Identify the blood parasite species.
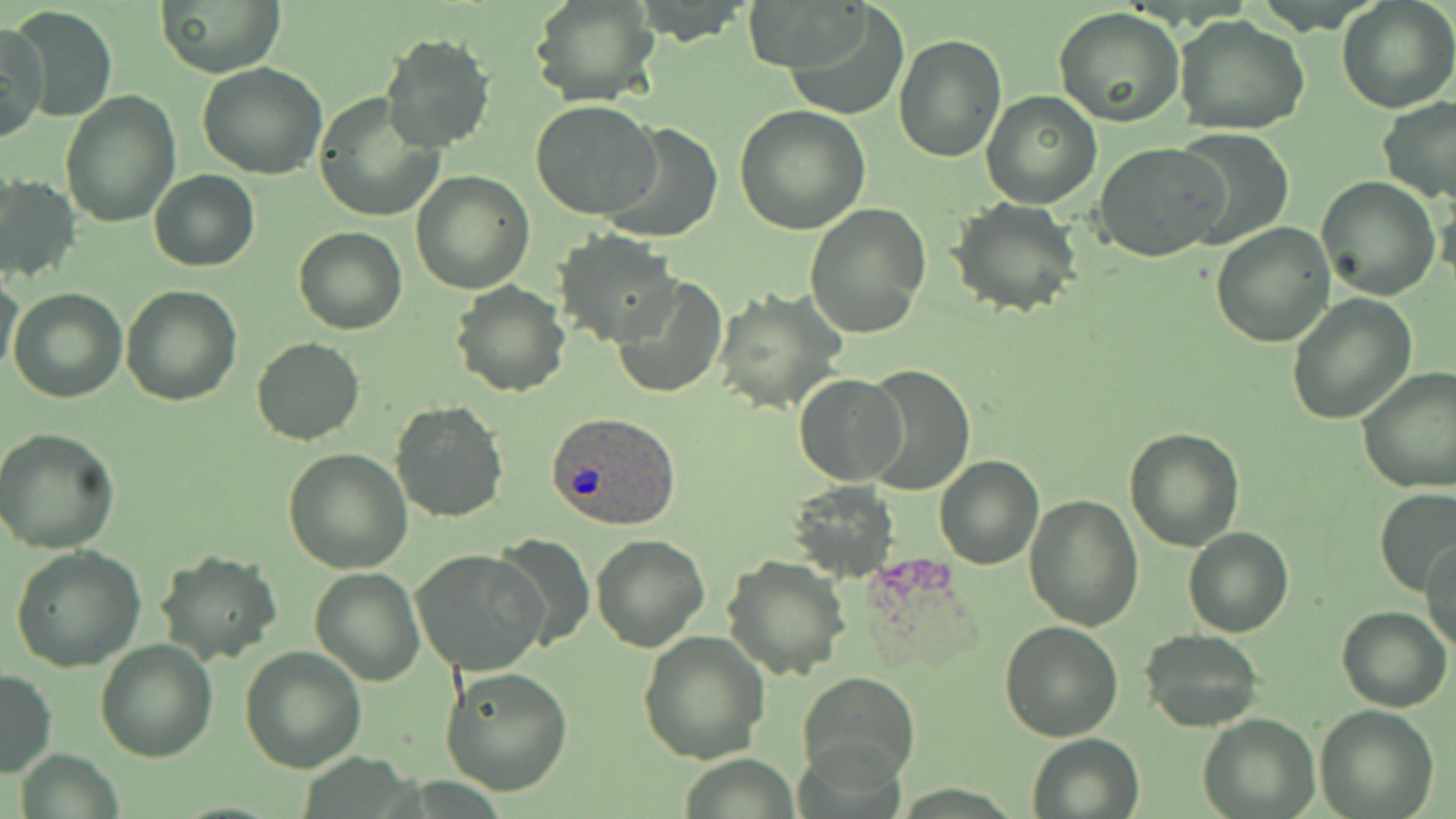

Plasmodium ovale.

{
  "preparation": "thin blood smear",
  "magnification": "1000x",
  "plasmodium_ovale_infected_red_blood_cell_locations": "approximate bounding boxes as named x1/y1/x2/y2 corners in pixels: (x1=547, y1=411, x2=682, y2=533)",
  "uninfected_red_blood_cell_locations": "approximate bounding boxes as named x1/y1/x2/y2 corners in pixels: (x1=745, y1=0, x2=873, y2=74), (x1=1337, y1=0, x2=1455, y2=112), (x1=154, y1=1, x2=287, y2=77), (x1=530, y1=1, x2=659, y2=108), (x1=784, y1=3, x2=911, y2=120), (x1=9, y1=6, x2=116, y2=124), (x1=1053, y1=8, x2=1186, y2=129), (x1=1174, y1=15, x2=1312, y2=136), (x1=1, y1=20, x2=48, y2=143), (x1=379, y1=33, x2=496, y2=153), (x1=892, y1=34, x2=1007, y2=162), (x1=197, y1=63, x2=329, y2=180), (x1=980, y1=89, x2=1104, y2=209), (x1=61, y1=92, x2=181, y2=228), (x1=313, y1=95, x2=444, y2=224), (x1=1377, y1=95, x2=1456, y2=204), (x1=531, y1=100, x2=661, y2=221), (x1=734, y1=104, x2=870, y2=234), (x1=602, y1=122, x2=723, y2=241), (x1=1168, y1=127, x2=1295, y2=250), (x1=1095, y1=142, x2=1226, y2=260), (x1=149, y1=169, x2=260, y2=272), (x1=410, y1=171, x2=534, y2=295), (x1=1, y1=174, x2=81, y2=284), (x1=1315, y1=177, x2=1440, y2=300), (x1=1434, y1=181, x2=1456, y2=285), (x1=948, y1=198, x2=1081, y2=317), (x1=804, y1=203, x2=931, y2=339), (x1=1211, y1=223, x2=1335, y2=348), (x1=293, y1=226, x2=406, y2=335), (x1=554, y1=232, x2=679, y2=346), (x1=0, y1=269, x2=24, y2=378), (x1=611, y1=275, x2=726, y2=399), (x1=450, y1=283, x2=570, y2=397), (x1=120, y1=285, x2=241, y2=405), (x1=9, y1=287, x2=126, y2=403), (x1=713, y1=287, x2=846, y2=414), (x1=1286, y1=293, x2=1419, y2=426), (x1=252, y1=337, x2=365, y2=446), (x1=861, y1=364, x2=975, y2=493), (x1=1355, y1=366, x2=1456, y2=494), (x1=794, y1=374, x2=907, y2=484), (x1=390, y1=399, x2=508, y2=522), (x1=0, y1=427, x2=121, y2=552), (x1=1124, y1=427, x2=1246, y2=551), (x1=283, y1=447, x2=413, y2=573), (x1=934, y1=455, x2=1044, y2=569), (x1=790, y1=482, x2=900, y2=579), (x1=1375, y1=486, x2=1455, y2=596), (x1=1023, y1=495, x2=1144, y2=632), (x1=1184, y1=527, x2=1293, y2=637), (x1=589, y1=534, x2=710, y2=654), (x1=491, y1=536, x2=594, y2=650), (x1=1421, y1=537, x2=1456, y2=654), (x1=10, y1=544, x2=147, y2=671), (x1=154, y1=550, x2=283, y2=664), (x1=411, y1=550, x2=547, y2=677), (x1=723, y1=554, x2=852, y2=680), (x1=308, y1=567, x2=425, y2=686), (x1=1336, y1=605, x2=1452, y2=712), (x1=1000, y1=621, x2=1124, y2=741), (x1=638, y1=629, x2=770, y2=764), (x1=1140, y1=629, x2=1266, y2=733), (x1=94, y1=639, x2=218, y2=761), (x1=239, y1=646, x2=366, y2=773), (x1=438, y1=667, x2=573, y2=794), (x1=0, y1=670, x2=58, y2=776), (x1=800, y1=670, x2=919, y2=783), (x1=1314, y1=704, x2=1439, y2=819), (x1=1199, y1=713, x2=1320, y2=819), (x1=1025, y1=734, x2=1144, y2=819), (x1=19, y1=749, x2=121, y2=817), (x1=679, y1=756, x2=800, y2=817)",
  "modality": "optical microscopy",
  "stain": "May-Grünwald-Giemsa",
  "field_of_view": "single",
  "image_size": "1456×819 pixels"
}